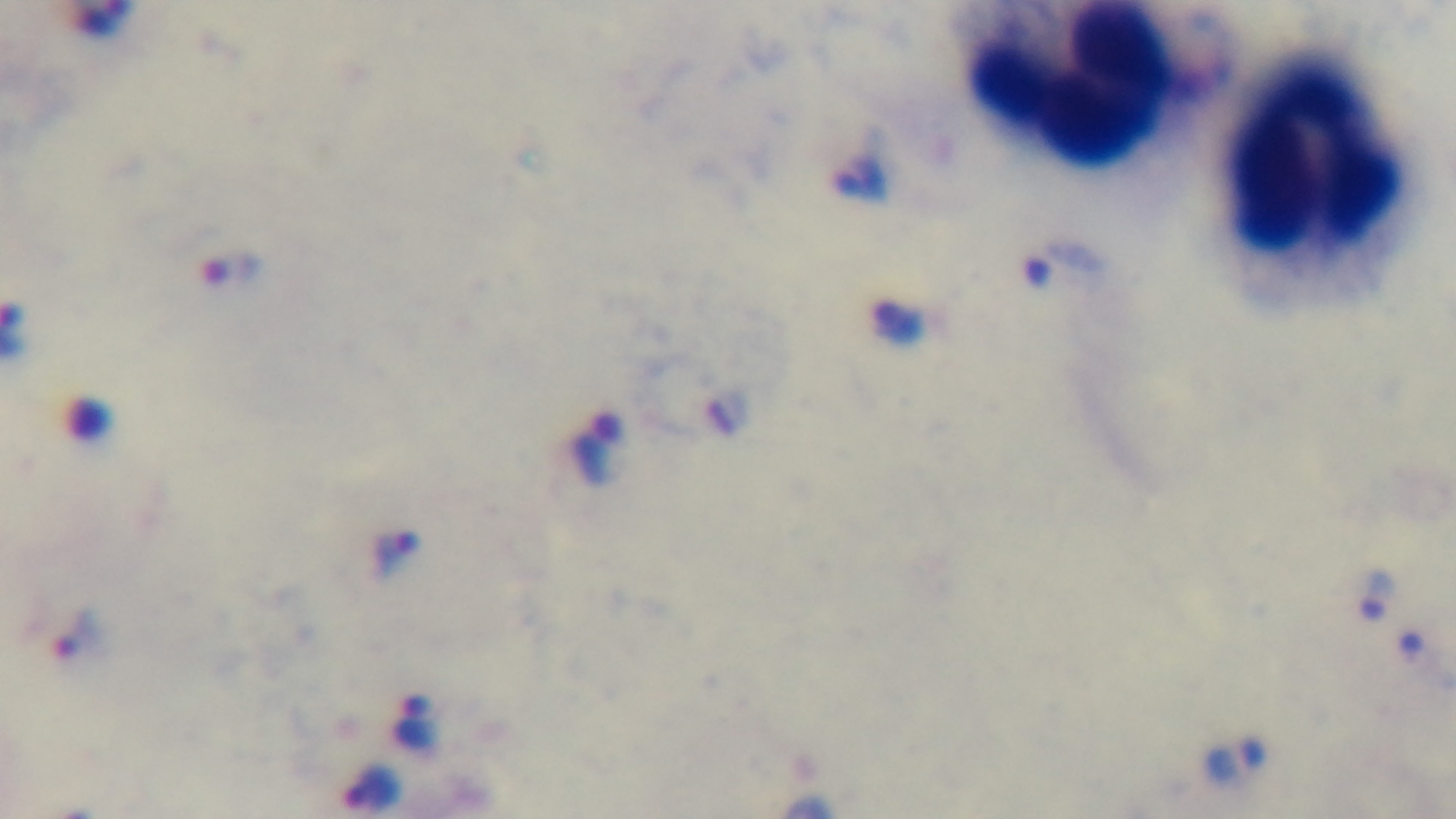

malaria status = positive
stain = Giemsa
capture = mounted 4K digital camera
field of view = single
preparation = thick
modality = light microscopy
objective = 100x oil immersion